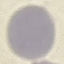 Result: no malaria parasites detected. Acquired by smartphone through the microscope eyepiece. Giemsa stain. Automatically extracted cell patch, resized to 64 × 64 pixels. Thin blood film.